Locate and identify every blood parasite.
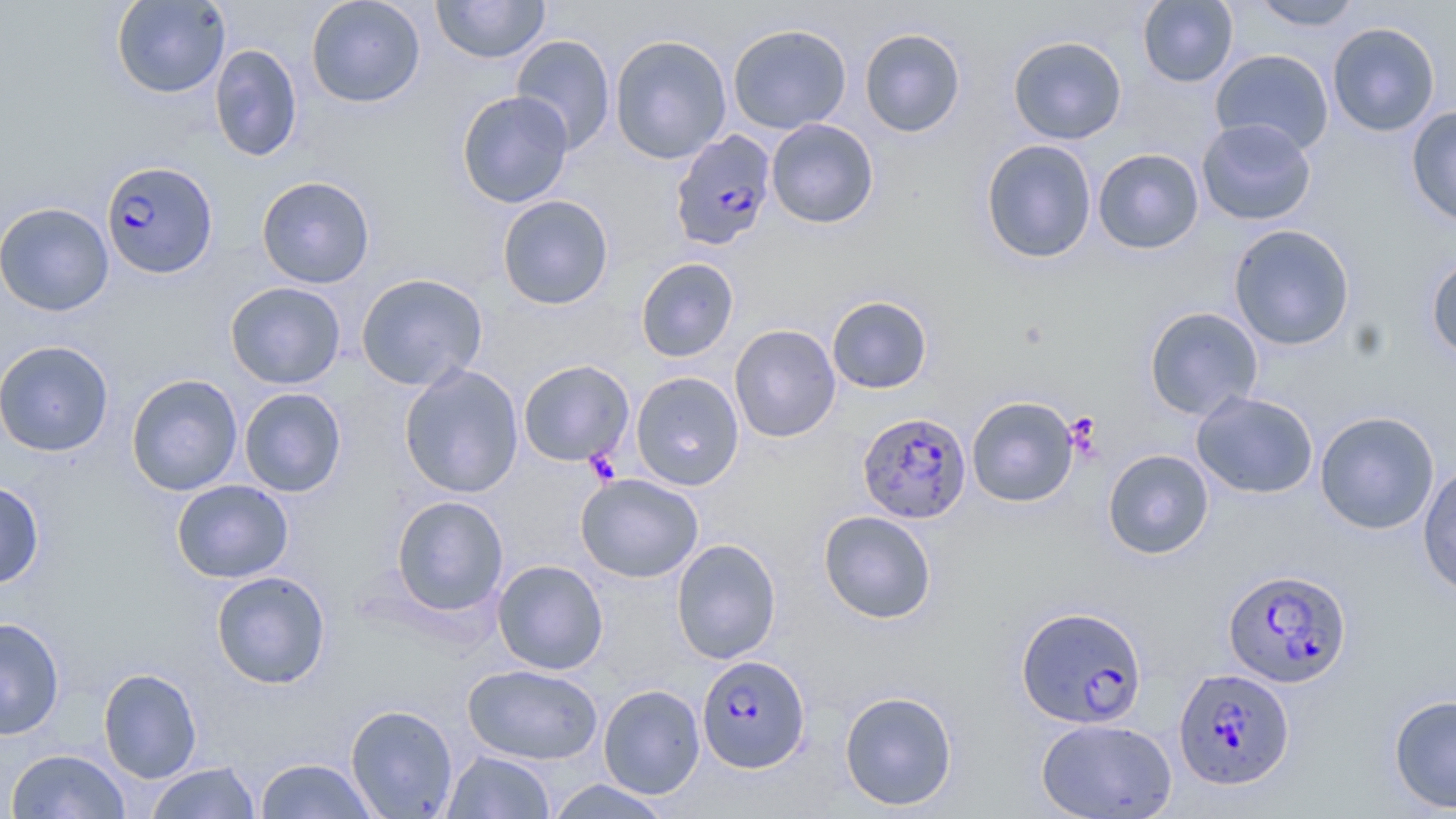
Approximate bounding boxes as (x1,y1)-(x2,y2) corner pairs in pixels.
Plasmodium falciparum-infected red blood cells: (669,130)-(778,251), (101,160)-(219,278), (855,410)-(971,527), (1222,567)-(1353,689), (1016,605)-(1148,729), (697,655)-(811,773), (1173,667)-(1296,790).
No Plasmodium ovale, Plasmodium malariae, Plasmodium vivax, Babesia divergens, or Trypanosoma brucei observed.

Summary:
  - Platelet locations: (584,449)-(621,485)
  - Uninfected red blood cell locations: (111,0)-(230,99), (305,0)-(426,108), (431,0)-(550,63), (1137,0)-(1238,88), (1250,0)-(1365,31), (1327,22)-(1440,136), (727,23)-(852,134), (859,27)-(966,137), (609,34)-(732,164), (511,35)-(616,155), (1008,35)-(1127,144), (209,44)-(303,162), (1210,49)-(1334,156), (456,90)-(574,208), (1406,106)-(1456,226), (766,118)-(879,228), (1196,118)-(1317,226), (980,139)-(1098,264), (1093,148)-(1204,254), (256,175)-(375,289), (497,195)-(614,310), (0,202)-(115,316), (1228,224)-(1355,350), (1425,253)-(1456,362), (635,257)-(739,362), (355,272)-(488,391), (225,282)-(346,389), (827,295)-(933,394), (1143,306)-(1263,420), (729,324)-(841,442), (0,340)-(114,456), (518,360)-(634,466), (399,364)-(524,498), (630,371)-(744,490), (125,373)-(243,496), (239,387)-(347,497), (1191,390)-(1319,499), (966,396)-(1079,507), (1314,410)-(1440,534), (1103,449)-(1214,559), (1417,462)-(1456,599), (576,473)-(703,583), (172,479)-(293,583), (0,480)-(44,589), (391,495)-(509,616), (818,510)-(937,623), (671,538)-(781,664), (492,559)-(608,675), (211,570)-(331,689), (0,617)-(66,740), (463,663)-(602,764), (98,667)-(202,783), (599,684)-(705,799), (839,690)-(958,811), (1388,693)-(1456,813), (345,704)-(459,818), (1036,717)-(1177,818), (6,748)-(130,819), (442,750)-(556,818), (255,758)-(378,819), (145,762)-(261,818), (545,779)-(674,818)
  - Slide-level diagnosis: Plasmodium falciparum
  - Preparation: thin blood film
  - Image size: 1456×819 pixels
  - Field of view: single
  - Stain: May-Grünwald-Giemsa
  - Magnification: 1000x
  - Modality: light microscopy